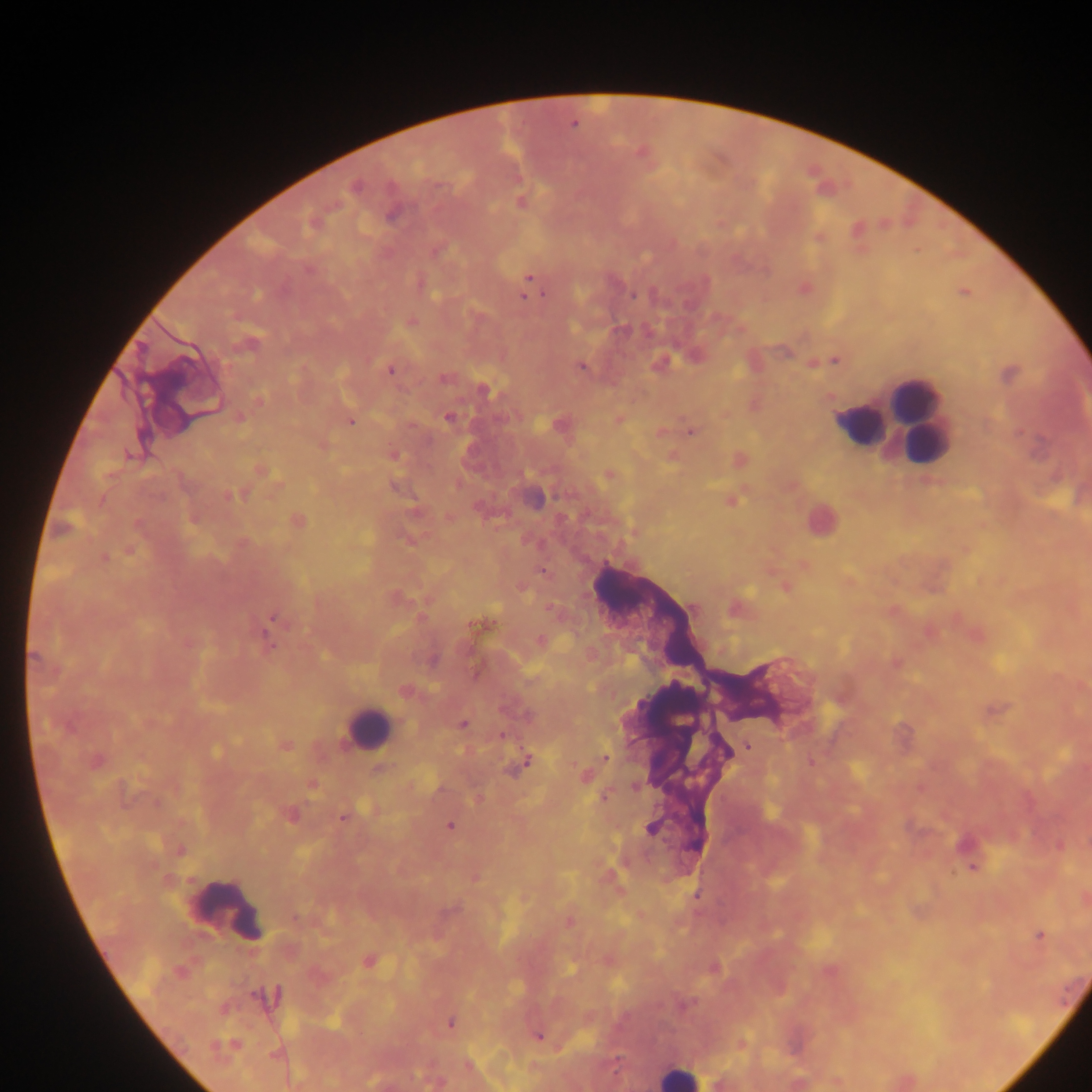
country: Ghana
preparation: thick blood smear
capture: mobile-phone photograph through a microscope
image_size: 1092×1092 pixels
leukocyte_locations: 'approximate centers as (x, y) in pixels: (913, 398), (917, 414), (859, 425), (368, 726), (230, 907), (678, 1076)'
plasmodium_parasite_locations: 'approximate centers as (x, y) in pixels: (574, 124), (355, 187), (522, 202), (392, 214), (308, 270), (529, 278), (544, 294), (634, 295), (524, 296), (412, 321), (248, 344), (835, 360), (581, 367), (390, 370), (444, 378), (483, 390), (259, 400), (448, 417), (239, 418), (351, 422), (691, 432), (129, 455), (261, 471), (609, 475), (230, 496), (102, 500), (732, 501), (299, 521), (633, 534), (130, 551), (104, 558), (805, 566), (542, 572), (784, 588), (273, 618), (474, 626), (270, 645), (34, 657), (895, 662), (407, 691), (463, 724), (503, 736), (286, 745), (748, 746), (605, 757), (527, 761), (97, 762), (811, 762), (380, 768), (585, 776), (312, 786), (635, 786), (603, 798), (290, 815), (343, 818), (449, 826), (650, 828), (180, 850), (972, 867), (697, 895), (569, 921), (1040, 935), (368, 962), (451, 1024), (538, 1037), (468, 1065)'
field_of_view: single